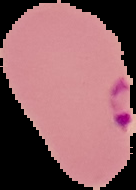

Summary:
  - Image type: segmented cell region with the area outside set to black
  - Preparation: thin blood smear
  - Result: Plasmodium parasites detected
  - Image size: 136×190 pixels